Name the cell type shown.
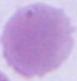
An erythrocyte.

1000x magnification. Micrograph.